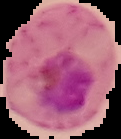 Result: malaria parasites identified. The area outside the segmented cell region is set to black. Image is 121×139 pixels. From a thin blood smear.